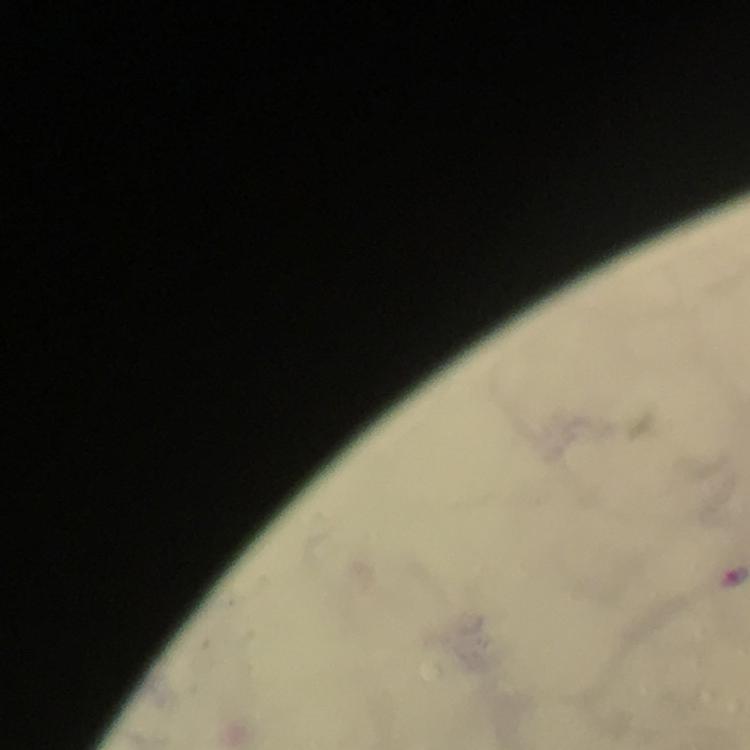

magnification: 100x
context: from a malaria diagnostic workup
image_size: 750×750 pixels
immersion_oil: used
malaria_parasite_locations: 'approximate centers as [x, y] in pixels: [736, 575]'
stain: Giemsa
preparation: thick smear
capture: smartphone mounted on the microscope
cropped_from: a single field of view